Assess this cell for malaria.
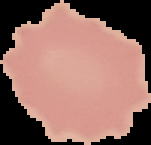

It is uninfected.

Segmented cell region on a black background. From a thin blood smear. Image is 151×145 pixels.